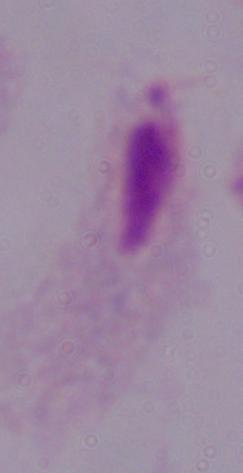
Summary:
  - Magnification: 1000x
  - Modality: micrograph
  - Identification: trichomonad